Report the malaria status of this cell.
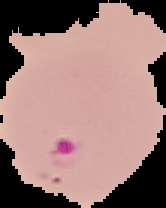
It is parasitized.

Summary:
  - Image size: 166×208 pixels
  - Preparation: thin blood smear
  - Image type: segmented cell region with the area outside set to black